Give the extent of all uninfected red blood cells.
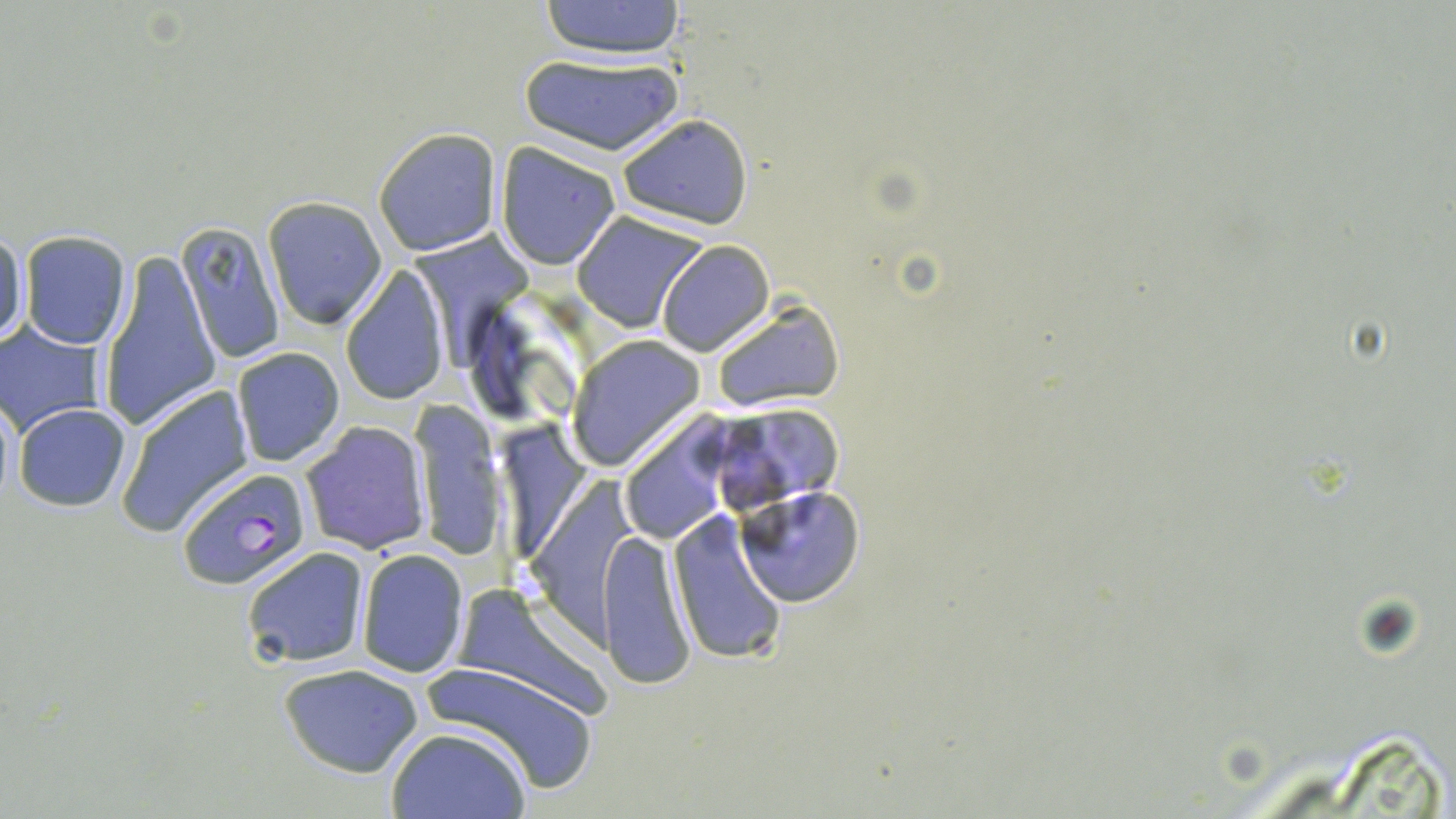
Approximate bounding boxes as [x1, y1, x2, y2] in pixels.
Uninfected red blood cells: [538, 0, 688, 59], [519, 53, 685, 155], [615, 113, 752, 230], [374, 130, 501, 255], [494, 144, 621, 268], [262, 197, 388, 331], [572, 212, 706, 332], [410, 220, 531, 372], [176, 221, 287, 364], [1, 226, 28, 349], [19, 230, 132, 349], [658, 241, 772, 355], [98, 248, 220, 435], [339, 269, 449, 407], [712, 302, 843, 409], [0, 322, 107, 436], [569, 338, 703, 468], [231, 346, 344, 467], [114, 383, 255, 537], [12, 402, 133, 512], [411, 404, 504, 561], [707, 406, 845, 512], [630, 410, 731, 546], [501, 419, 591, 556], [300, 421, 431, 555], [525, 473, 641, 659], [735, 485, 864, 607], [668, 512, 789, 666], [600, 531, 697, 689], [242, 546, 371, 669], [355, 549, 467, 678], [452, 584, 605, 717], [420, 658, 604, 794], [280, 663, 422, 779], [385, 726, 532, 819].

Summary:
  - Plasmodium falciparum-infected red blood cell locations: [175, 468, 314, 591]
  - Slide-level diagnosis: Plasmodium falciparum
  - Stain: May-Grünwald-Giemsa
  - Field of view: single
  - Magnification: 1000x
  - Modality: light microscopy
  - Preparation: thin blood film
  - Image size: 1456×819 pixels